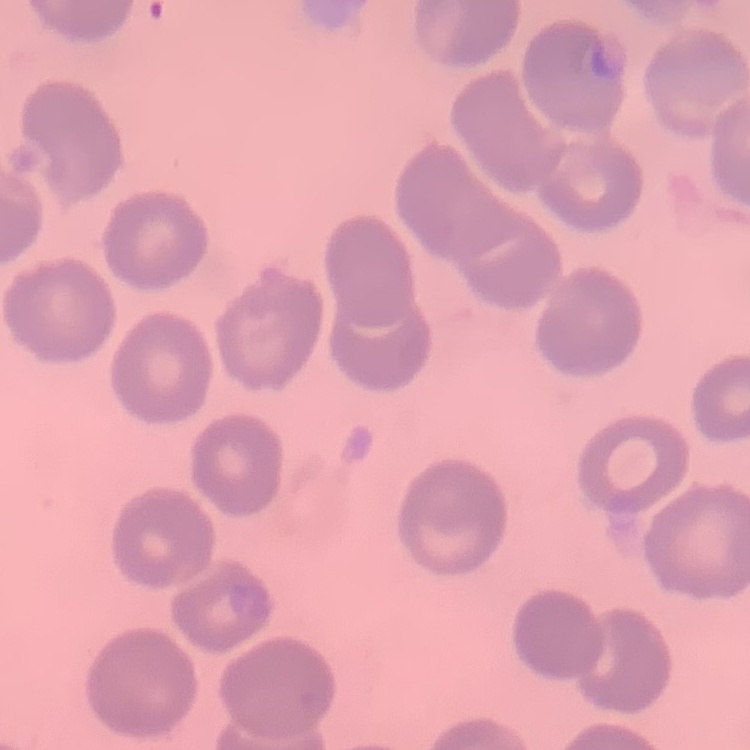

red blood cell morphology = no rouleaux formation
preparation = thin blood smear
stain = Field's or Giemsa
image type = one tile cut from a larger photomicrograph